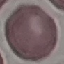
malaria status = uninfected
stain = Giemsa
capture = smartphone camera at the microscope eyepiece
image type = cell patch, automatically extracted from a larger field of view and resized to 64 × 64 pixels
preparation = thin smear